Assess the morphology of the red blood cells.
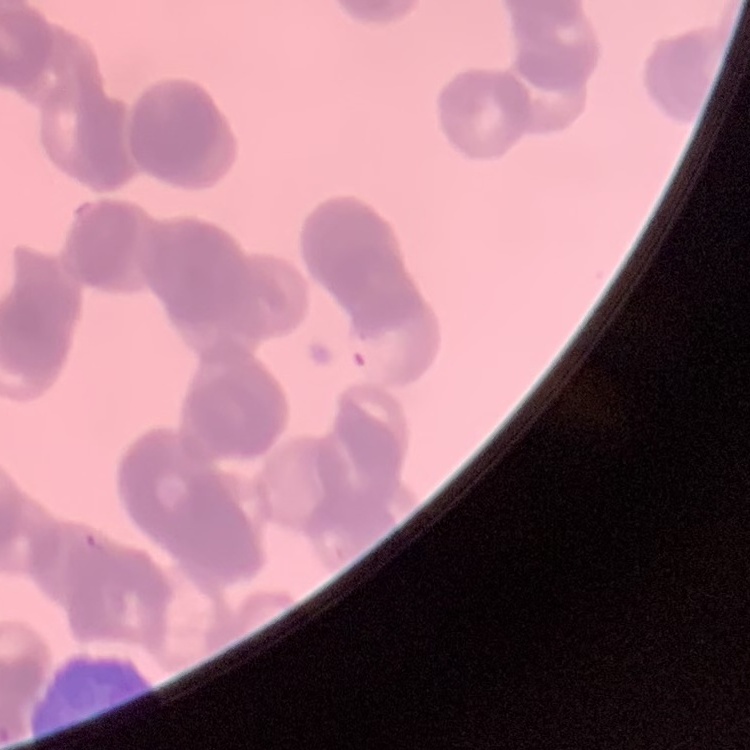

They show rouleaux formation.

One tile cut from a larger photomicrograph. Thin peripheral smear. Field's or Giemsa stain.